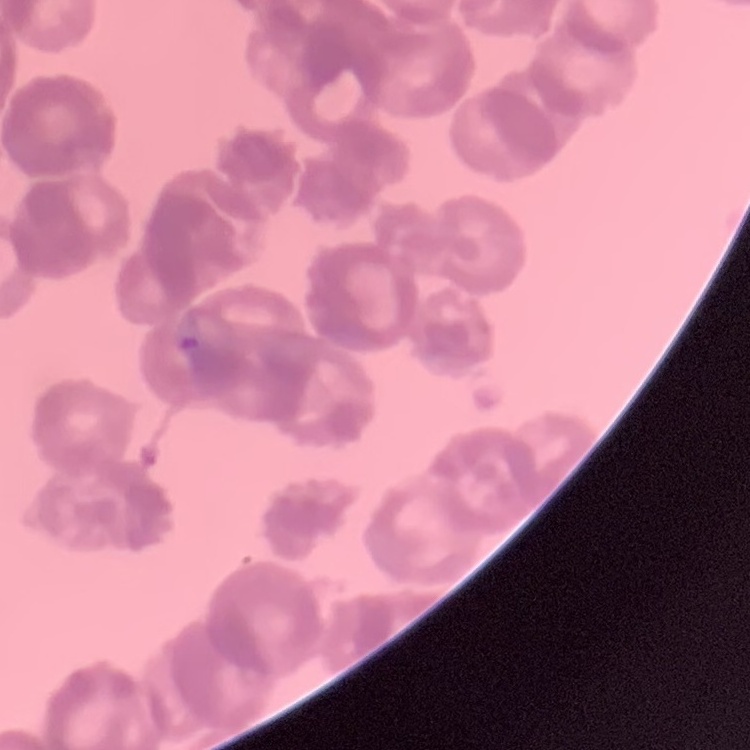
red blood cell morphology = rouleaux formation
preparation = thin blood film
image type = one tile cut from a larger photomicrograph
stain = Field's or Giemsa